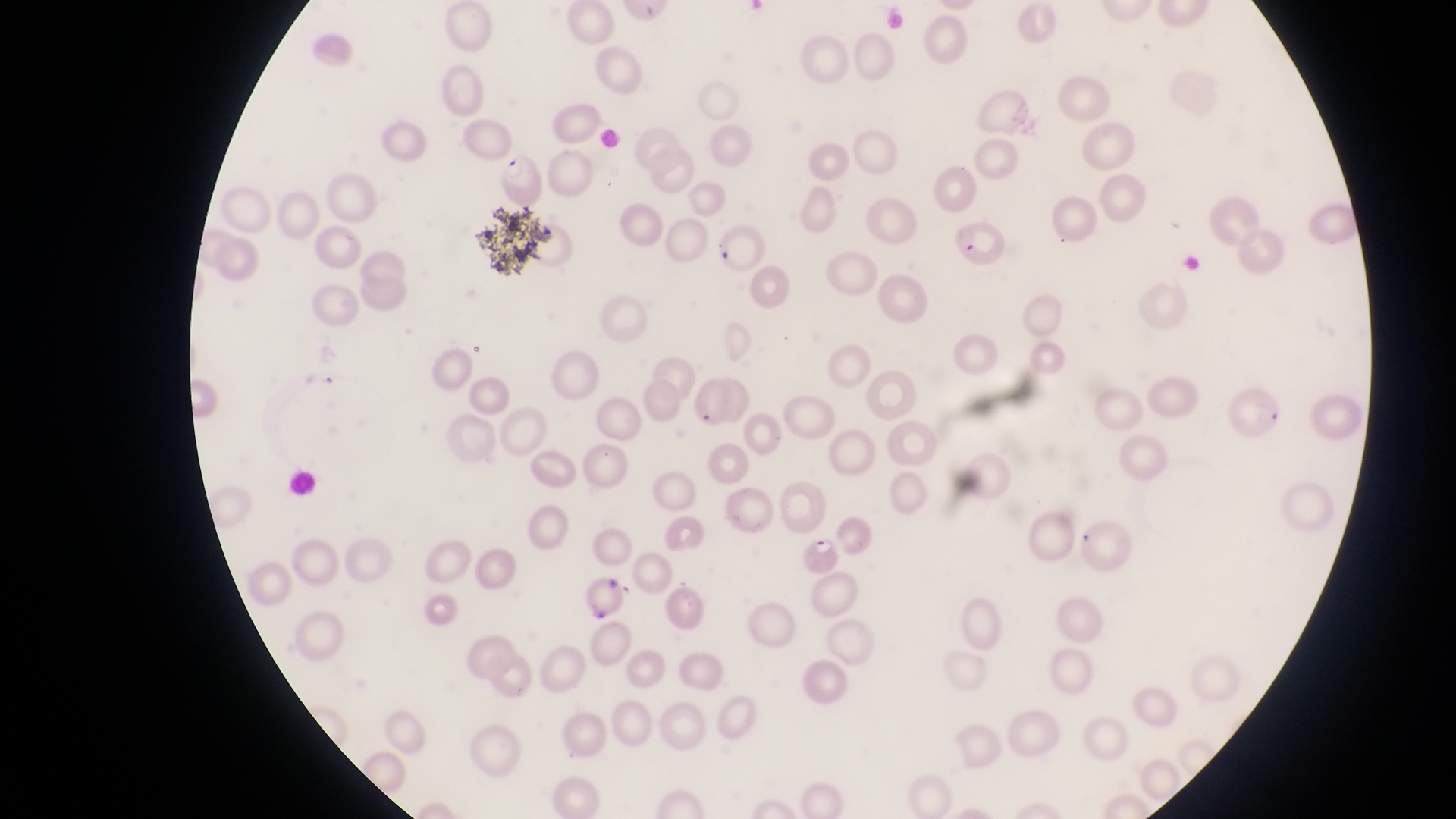

Approximate bounding boxes as [left, top, right, bottom] in pixels. Parasitised red blood cell locations: [497, 153, 549, 205], [944, 222, 1008, 274], [798, 528, 847, 575]. Artifact (platelet-like body, stain precipitate, or debris) locations: [589, 598, 619, 625]. Thin blood film. Collected in Uganda. At a magnification of 1000x. Captured by a smartphone held over the eyepiece of an Olympus CX-23 microscope. One field of view. Image is 1456×819 pixels.